Classify this cell by malaria status.
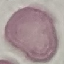
Uninfected.

stain = Giemsa
preparation = thin blood film
image type = automatically extracted cell patch, resized to 64 × 64 pixels
capture = smartphone camera at the microscope eyepiece